Give the extent of all uninfected red blood cells.
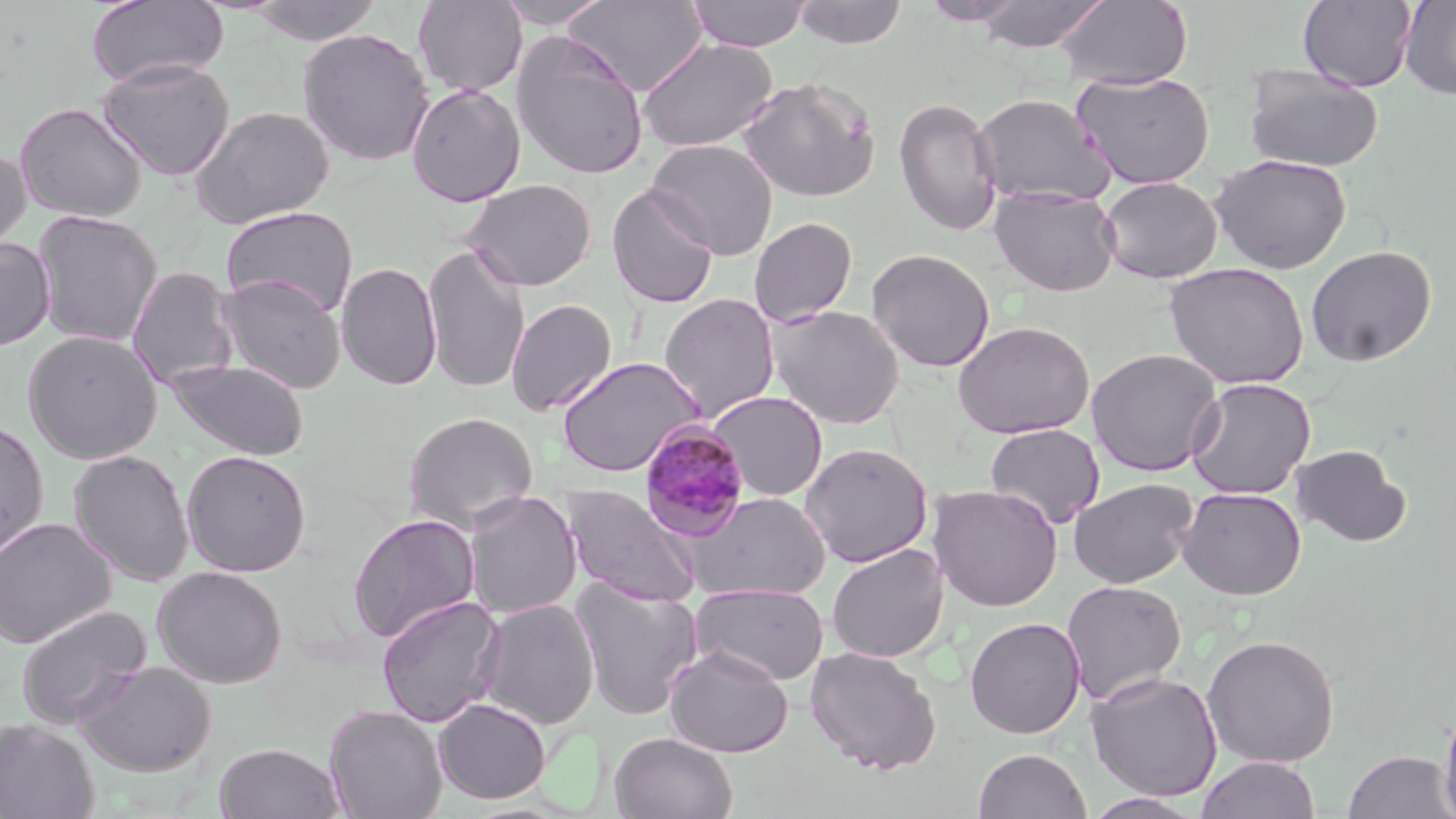

Approximate bounding boxes as (x1,y1)-(x2,y2) corner pairs in pixels.
Uninfected red blood cells: (86,0)-(228,89), (247,0)-(385,45), (494,0)-(614,28), (564,0)-(707,96), (687,0)-(811,51), (791,0)-(908,48), (973,0)-(1112,52), (1055,0)-(1193,89), (1297,0)-(1417,92), (1400,0)-(1456,101), (414,1)-(527,97), (921,1)-(1027,26), (298,28)-(435,166), (512,31)-(650,180), (638,38)-(777,152), (98,59)-(235,180), (1243,64)-(1384,173), (1072,70)-(1214,189), (738,75)-(881,203), (407,83)-(525,207), (972,93)-(1115,207), (893,96)-(1003,237), (15,101)-(147,223), (191,105)-(334,229), (646,138)-(778,259), (0,145)-(31,257), (1210,153)-(1352,273), (1097,176)-(1223,284), (462,178)-(597,290), (606,184)-(720,310), (989,186)-(1122,297), (221,206)-(358,318), (32,210)-(162,347), (748,216)-(859,328), (0,236)-(56,351), (422,242)-(531,395), (1305,245)-(1437,367), (865,248)-(996,372), (337,261)-(443,391), (1164,262)-(1310,389), (127,266)-(239,390), (216,274)-(347,394), (659,293)-(781,423), (505,298)-(618,416), (767,304)-(905,429), (952,320)-(1095,438), (22,330)-(163,464), (1087,348)-(1223,477), (556,356)-(706,477), (165,358)-(310,461), (1185,378)-(1316,499), (706,390)-(828,502), (403,411)-(539,531), (0,418)-(50,561), (985,423)-(1105,529), (799,442)-(934,567), (1290,444)-(1411,548), (69,448)-(195,587), (182,449)-(311,577), (1068,477)-(1198,588), (562,484)-(702,607), (928,484)-(1063,612), (1176,486)-(1307,600), (463,490)-(582,620), (686,491)-(831,600), (347,512)-(481,644), (0,517)-(116,648), (826,543)-(949,663), (152,565)-(288,688), (570,577)-(704,720), (1061,580)-(1187,706), (690,582)-(829,685), (377,594)-(505,728), (477,598)-(600,730), (16,605)-(152,729), (964,616)-(1086,739), (1202,634)-(1340,767), (664,643)-(794,757), (805,645)-(943,774), (77,661)-(216,776), (1085,670)-(1223,802), (433,698)-(551,804), (1438,698)-(1456,819), (324,705)-(448,819), (0,718)-(99,819), (611,732)-(737,819), (214,743)-(346,819), (973,748)-(1091,819), (1342,750)-(1454,818), (1196,755)-(1321,819), (1081,792)-(1208,818).

Summary:
  - Plasmodium malariae-infected red blood cell locations: (639,421)-(752,541)
  - Slide-level diagnosis: Plasmodium malariae
  - Field of view: single
  - Modality: light microscopy
  - Magnification: 1000x
  - Stain: May-Grünwald-Giemsa
  - Image size: 1456×819 pixels
  - Preparation: thin blood film